State the preparation type.
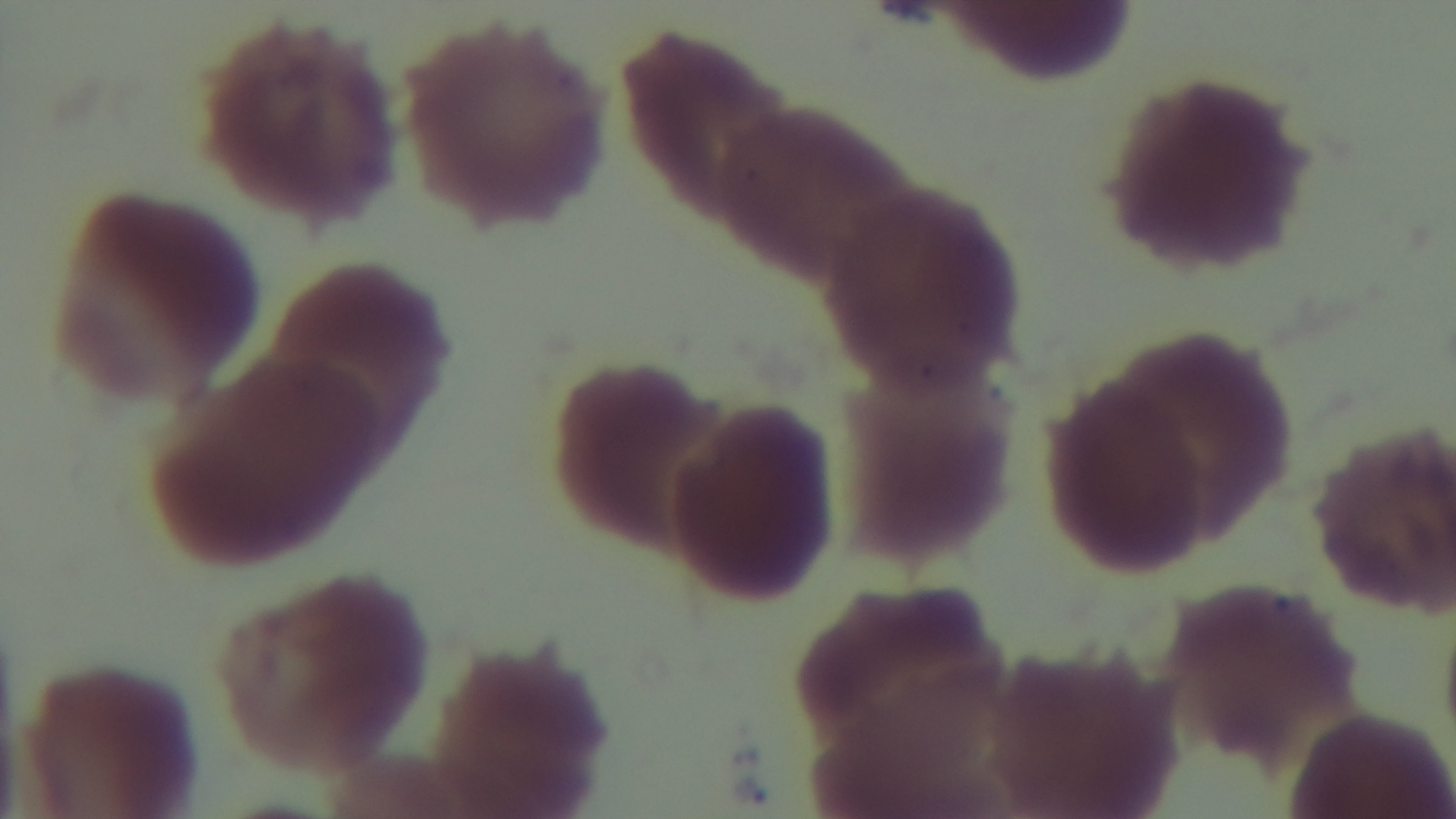

It is a thin blood film.

modality = light microscopy
malaria status = uninfected
stain = Giemsa
field of view = single
objective = 100x oil immersion
capture = mounted 4K digital camera